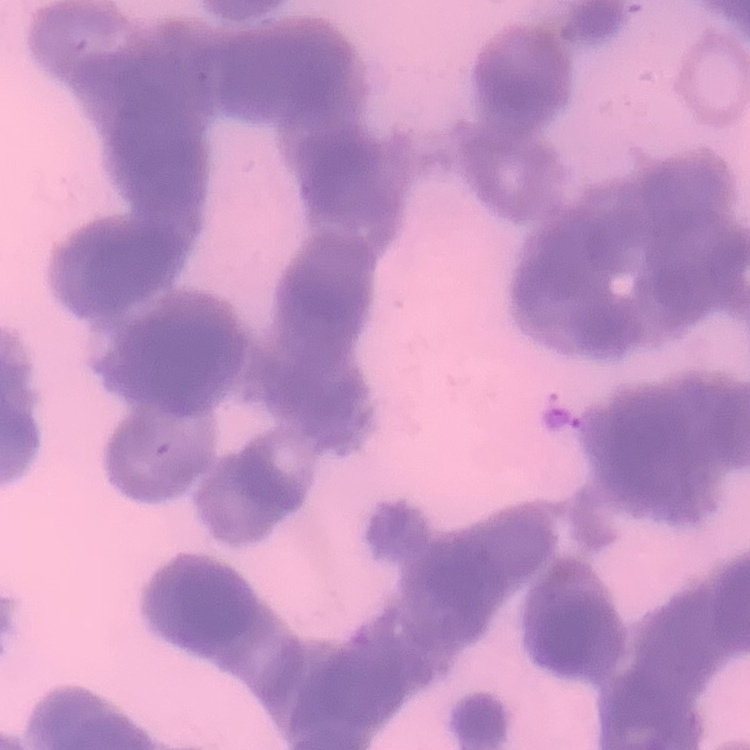

Summary:
  - Red blood cell morphology: rouleaux formation
  - Image type: square crop of a larger photomicrograph
  - Stain: Field's or Giemsa
  - Preparation: thin peripheral smear